Name the parasite shown.
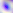

Toxoplasma gondii.

Captured at 400x magnification. Photomicrograph.